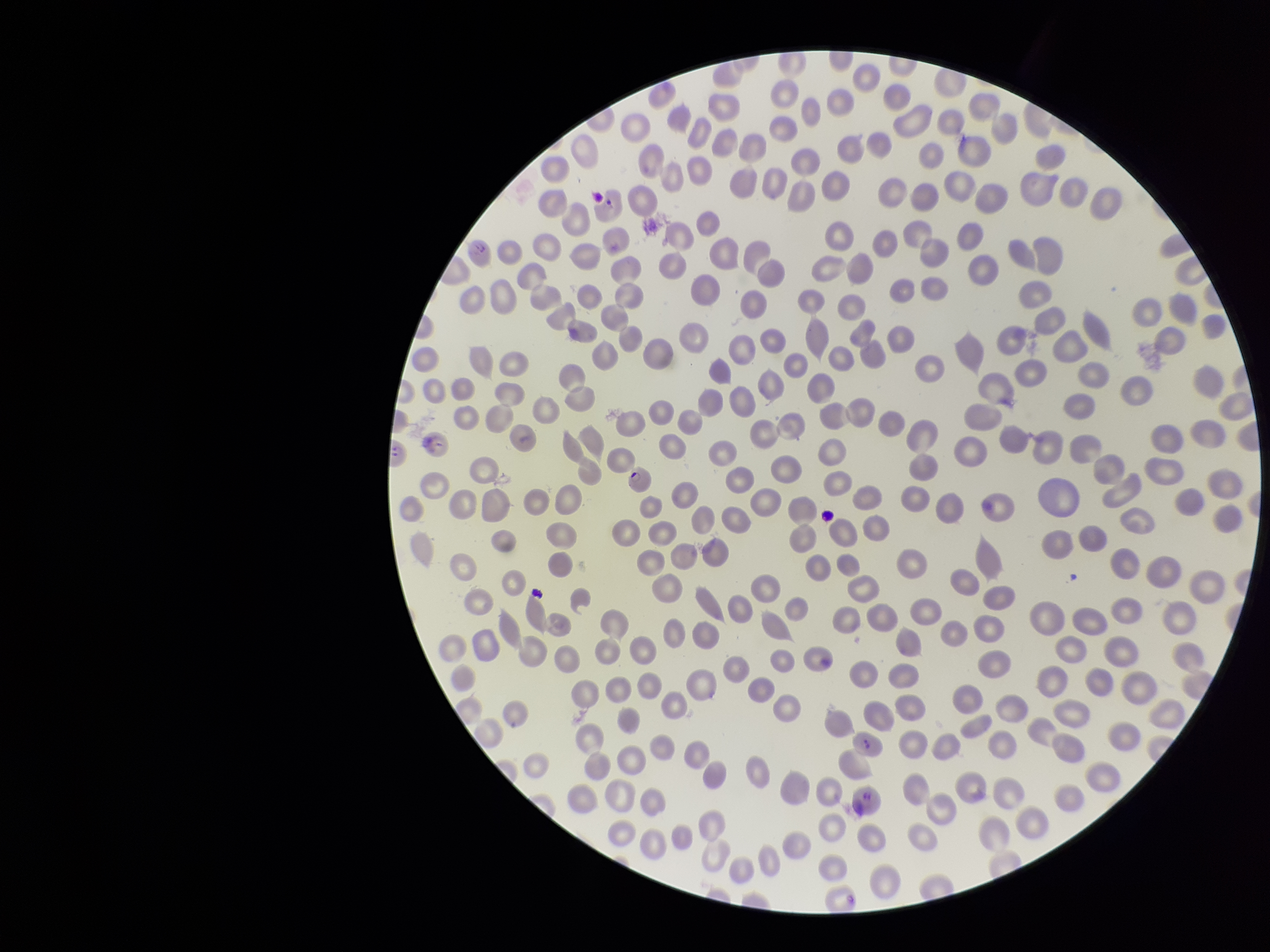

Summary:
  - Parasitized red blood cell count: 3
  - Preparation: thin blood smear
  - Stain: Giemsa
  - Red blood cell count: 286
  - Patient malaria status: positive
  - Parasitized red blood cells: detected
  - Capture: smartphone photograph through the microscope eyepiece
  - Field of view: single
  - Species reported for this patient: Plasmodium falciparum
  - Image size: 1270×952 pixels